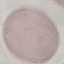

Summary:
  - Result: no malaria parasites detected
  - Stain: Giemsa
  - Image type: cell patch, automatically extracted from a larger field of view and resized to 64 × 64 pixels
  - Preparation: thin blood film
  - Capture: smartphone through the microscope eyepiece